Identify the parasite.
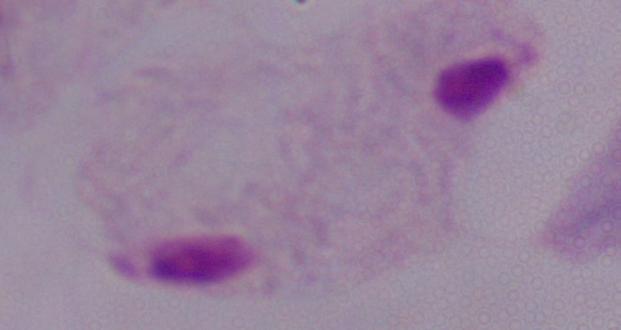

This is a trichomonad.

Micrograph. 1000x magnification.